Locate every malaria parasite.
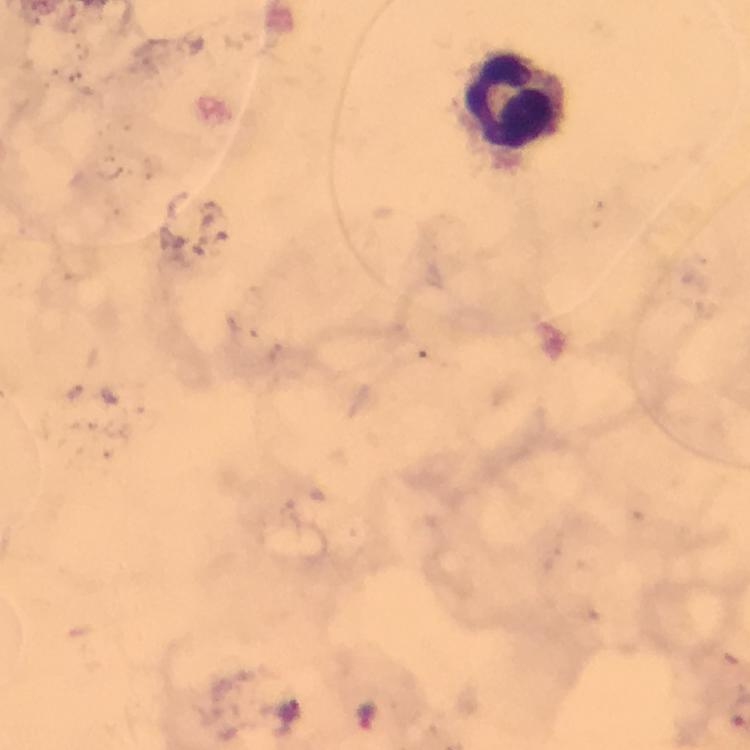
Approximate centers as (x, y) in pixels.
Malaria parasites: (367, 714).

Leukocyte locations: (516, 103). Photographed through the microscope with a smartphone camera. Image is 750×750 pixels. Cropped region of a single field of view. Thick blood film. Giemsa stain. From a malaria diagnostic workup. 100x magnification. Immersion oil was used.